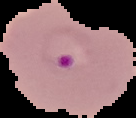

The area outside the segmented cell region is set to black. Image is 136×118 pixels. Result: malaria parasites detected. From a thin blood smear.